Outline each uninfected red blood cell.
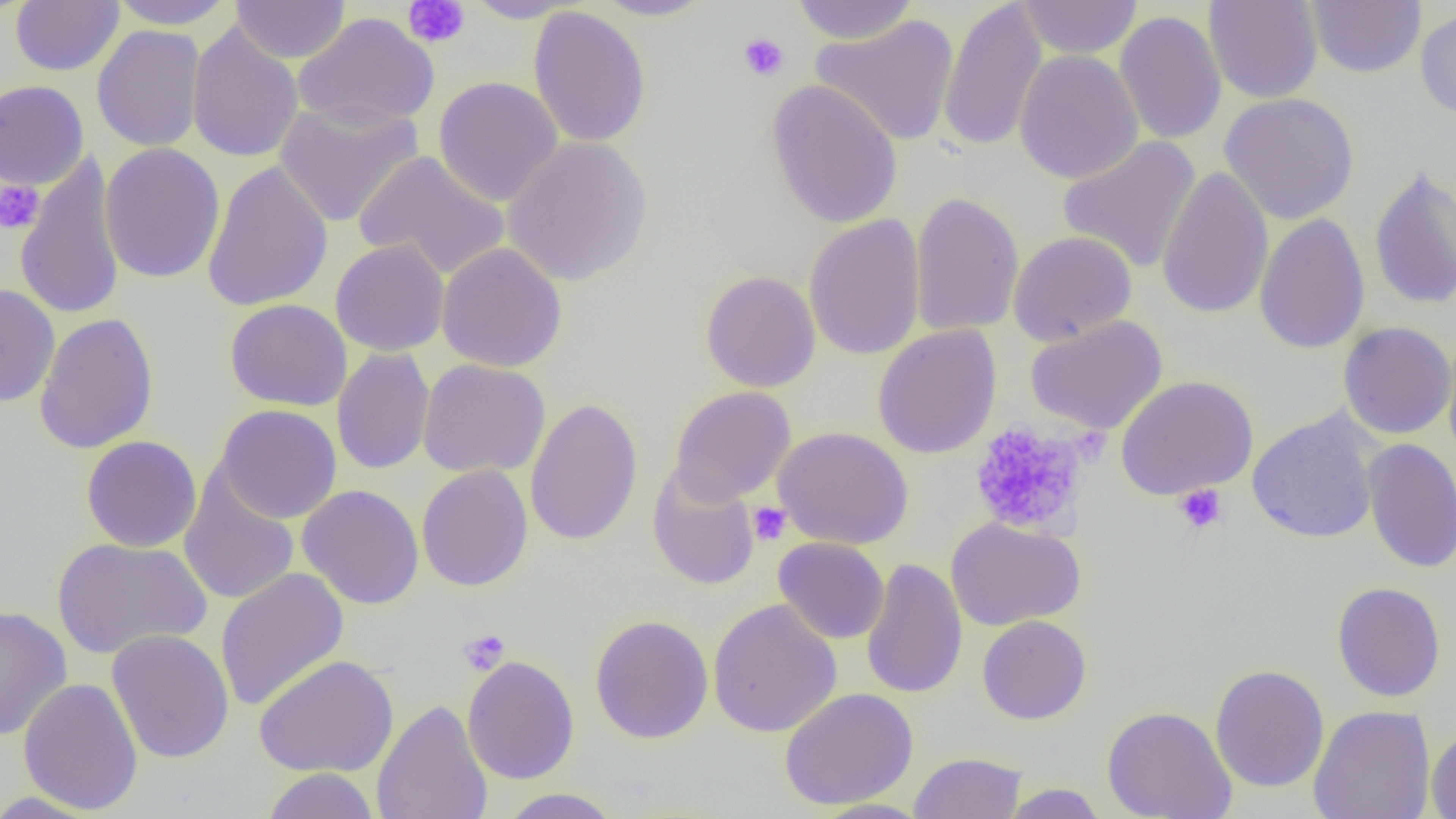
Approximate bounding boxes as (x1,y1)-(x2,y2) corner pairs in pixels.
Uninfected red blood cells: (10,0)-(124,76), (108,0)-(236,30), (463,0)-(585,23), (593,0)-(715,21), (790,0)-(921,44), (938,0)-(1048,153), (1016,0)-(1143,59), (1203,0)-(1323,104), (1306,0)-(1426,78), (231,1)-(350,64), (528,6)-(651,148), (1415,8)-(1456,119), (1114,10)-(1227,145), (293,12)-(439,132), (811,15)-(959,146), (187,22)-(304,163), (92,24)-(207,152), (1014,50)-(1144,185), (434,76)-(563,207), (765,79)-(903,229), (0,80)-(89,189), (1220,92)-(1359,224), (274,99)-(423,228), (502,135)-(654,287), (1058,136)-(1202,274), (99,142)-(225,284), (353,150)-(509,281), (14,153)-(126,321), (202,160)-(334,312), (1368,163)-(1456,312), (1156,165)-(1273,319), (910,191)-(1024,336), (1253,213)-(1370,355), (804,214)-(926,361), (1008,230)-(1137,345), (331,239)-(449,357), (436,242)-(568,372), (700,270)-(821,392), (0,283)-(60,408), (225,299)-(352,411), (33,312)-(159,455), (1025,315)-(1168,435), (1338,321)-(1456,440), (872,325)-(1002,459), (1441,333)-(1456,463), (332,347)-(435,476), (417,359)-(551,479), (1115,375)-(1258,500), (669,386)-(796,505), (524,397)-(643,546), (215,404)-(342,523), (1246,409)-(1382,544), (773,426)-(913,549), (80,435)-(202,552), (1361,438)-(1456,573), (417,464)-(533,592), (647,465)-(761,590), (179,470)-(300,606), (297,484)-(425,609), (946,517)-(1085,630), (51,536)-(212,660), (773,537)-(890,644), (860,558)-(968,699), (214,567)-(349,712), (1332,581)-(1446,702), (707,598)-(842,738), (0,604)-(72,741), (590,615)-(714,744), (977,615)-(1091,724), (106,629)-(234,764), (253,654)-(399,777), (462,654)-(579,784), (1210,663)-(1329,793), (18,677)-(143,814), (779,688)-(919,810), (372,699)-(493,819), (1102,705)-(1237,819), (1308,705)-(1436,819), (1426,727)-(1456,818), (909,752)-(1026,819), (261,768)-(380,819), (1001,783)-(1108,818), (496,788)-(624,818), (0,791)-(105,818), (811,798)-(932,819).

Summary:
  - Platelet locations: (403,0)-(470,48), (738,31)-(790,81), (0,180)-(45,234), (968,420)-(1089,539), (1173,484)-(1227,534), (747,501)-(792,546), (458,628)-(510,675)
  - Slide-level diagnosis: no evidence of blood parasites
  - Image size: 1456×819 pixels
  - Preparation: thin blood smear
  - Field of view: one of a larger specimen
  - Modality: optical microscopy
  - Magnification: 1000x